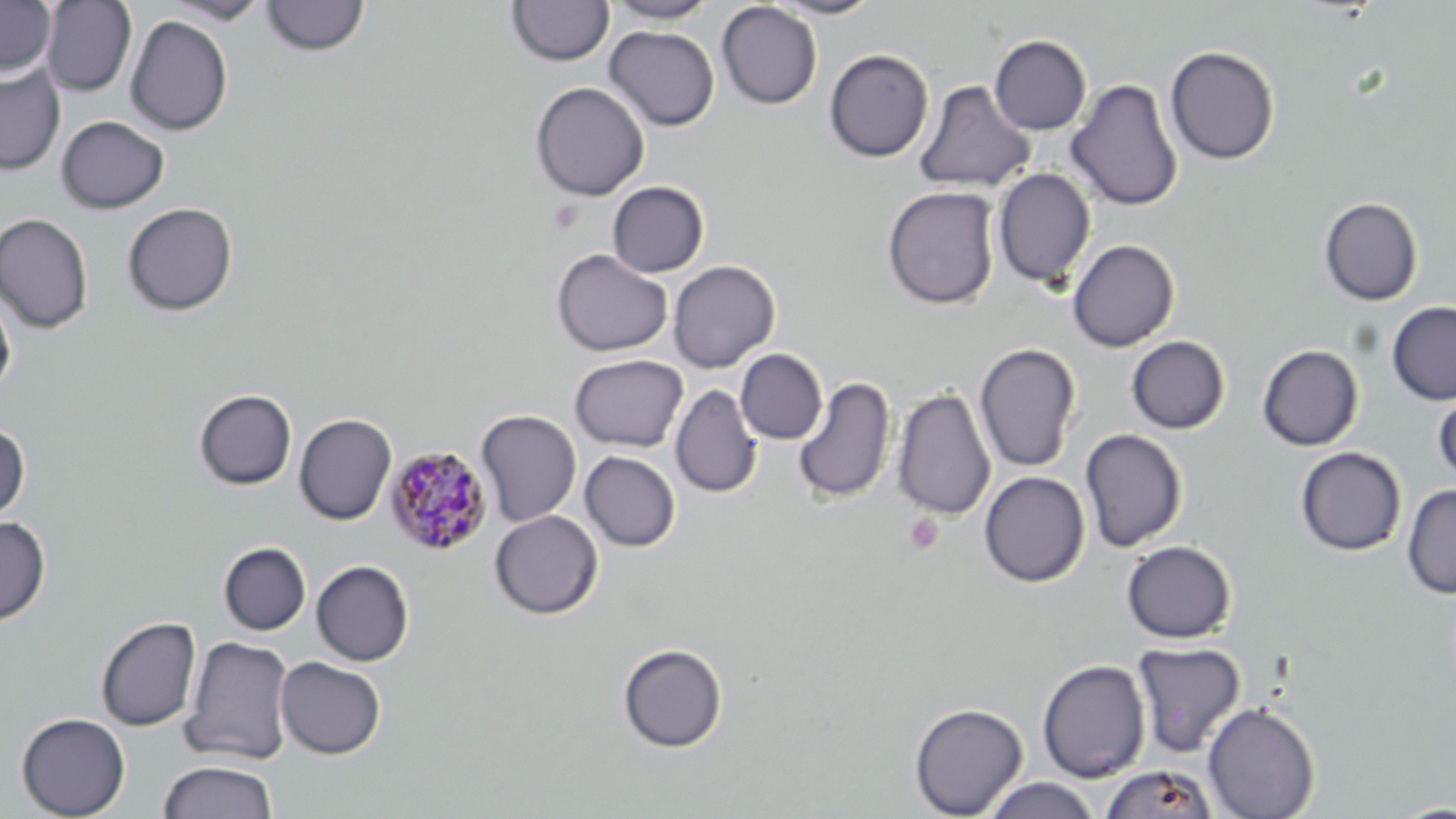

Summary:
  - Coordinate format: approximate bounding boxes as (x1, y1, x2, y2) in pixels
  - Uninfected red blood cell locations: (0, 0, 56, 77), (41, 0, 137, 97), (159, 0, 272, 24), (507, 0, 614, 66), (604, 0, 719, 24), (767, 0, 883, 19), (262, 1, 369, 57), (716, 2, 822, 109), (125, 15, 233, 135), (604, 25, 720, 131), (989, 35, 1092, 135), (1165, 45, 1280, 165), (824, 49, 934, 162), (0, 65, 65, 175), (1066, 78, 1183, 212), (913, 80, 1035, 193), (530, 81, 650, 201), (56, 115, 169, 213), (993, 168, 1096, 288), (607, 181, 709, 277), (882, 186, 1000, 309), (1319, 197, 1424, 305), (122, 202, 238, 316), (0, 213, 94, 333), (1067, 239, 1180, 352), (552, 249, 672, 356), (668, 260, 780, 373), (0, 291, 16, 397), (1386, 302, 1456, 404), (1125, 335, 1231, 434), (974, 342, 1082, 473), (1257, 344, 1364, 451), (736, 349, 827, 445), (570, 354, 689, 452), (793, 376, 896, 504), (1433, 382, 1456, 487), (670, 384, 763, 498), (892, 388, 996, 520), (194, 389, 297, 490), (475, 409, 582, 527), (294, 414, 397, 525), (0, 424, 30, 523), (1079, 428, 1188, 551), (1295, 446, 1407, 556), (580, 451, 681, 552), (979, 470, 1090, 587), (1402, 484, 1456, 598), (489, 510, 603, 619), (0, 516, 50, 625), (1121, 540, 1236, 643), (219, 542, 311, 634), (293, 559, 396, 758), (311, 560, 414, 666), (95, 615, 202, 731), (181, 636, 296, 764), (1131, 641, 1246, 757), (617, 643, 728, 753), (276, 656, 386, 759), (1037, 659, 1151, 783), (1203, 701, 1320, 819), (909, 702, 1029, 819), (16, 712, 130, 818), (158, 760, 278, 819), (1100, 764, 1219, 819), (982, 777, 1102, 818), (1390, 801, 1456, 818)
  - Platelet locations: (904, 513, 944, 554)
  - Plasmodium malariae-infected red blood cell locations: (384, 446, 492, 556)
  - Slide-level diagnosis: Plasmodium malariae
  - Modality: optical microscopy
  - Image size: 1456×819 pixels
  - Preparation: thin blood smear
  - Stain: May-Grünwald-Giemsa
  - Magnification: 1000x
  - Field of view: one of a larger specimen